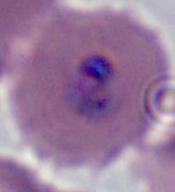
magnification = 400x or 1000x
identification = Plasmodium
modality = micrograph